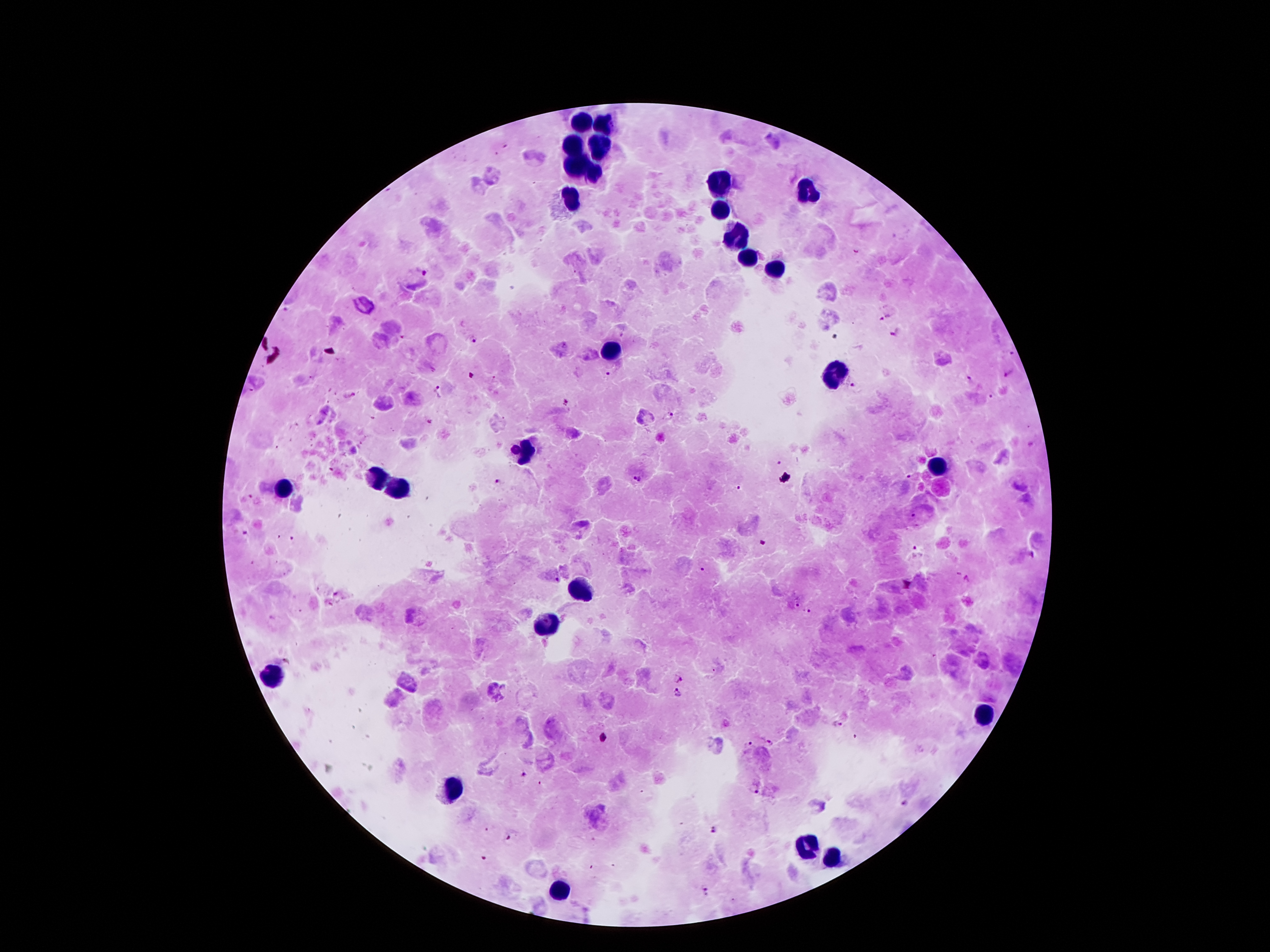

{
  "image_size": "1270×952 pixels",
  "capture": "smartphone camera through the microscope eyepiece",
  "field_of_view": "one from this slide",
  "plasmodium_parasite_locations": "approximate centers as [x, y] in pixels: [854, 251], [426, 273], [885, 317], [898, 334], [475, 340], [1014, 352], [607, 374], [970, 377], [1006, 377], [853, 387], [436, 391], [348, 396], [989, 396], [565, 399], [668, 416], [429, 423], [639, 475], [496, 483], [738, 488], [249, 498], [243, 532], [293, 539], [917, 554], [701, 567], [557, 579], [338, 594], [327, 604], [794, 606], [809, 613], [676, 678], [678, 693], [838, 727], [853, 735], [770, 742], [748, 745], [523, 773], [755, 791], [904, 802], [713, 830], [508, 836], [705, 891]",
  "stain": "Giemsa",
  "leukocyte_locations": "approximate centers as [x, y] in pixels: [584, 120], [602, 122], [572, 140], [600, 144], [570, 163], [595, 174], [720, 181], [808, 190], [572, 197], [720, 210], [738, 240], [749, 258], [777, 267], [606, 349], [833, 371], [522, 451], [938, 465], [372, 478], [391, 485], [282, 489], [581, 587], [547, 626], [270, 676], [988, 714], [452, 787], [804, 848], [833, 860], [559, 891]",
  "patient_malaria_status": "infected with Plasmodium falciparum",
  "preparation": "thick blood film",
  "magnification": "100x"
}